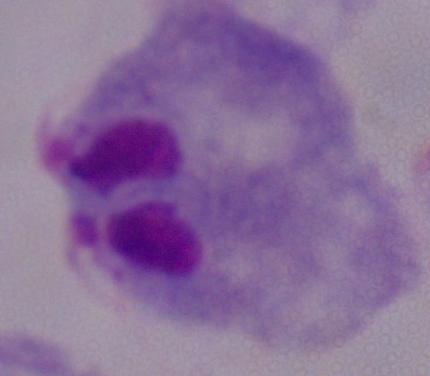
Summary:
  - Modality: photomicrograph
  - Identification: trichomonad
  - Magnification: 1000x